Assess the morphology of the erythrocytes.
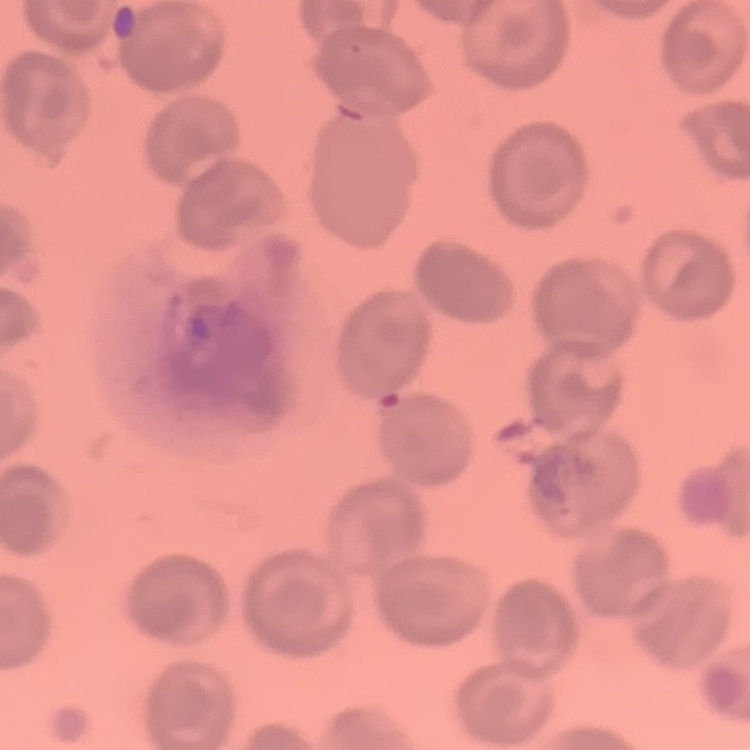
No rouleaux formation.

Field's or Giemsa stain. One tile cut from a larger photomicrograph. Thin blood film.